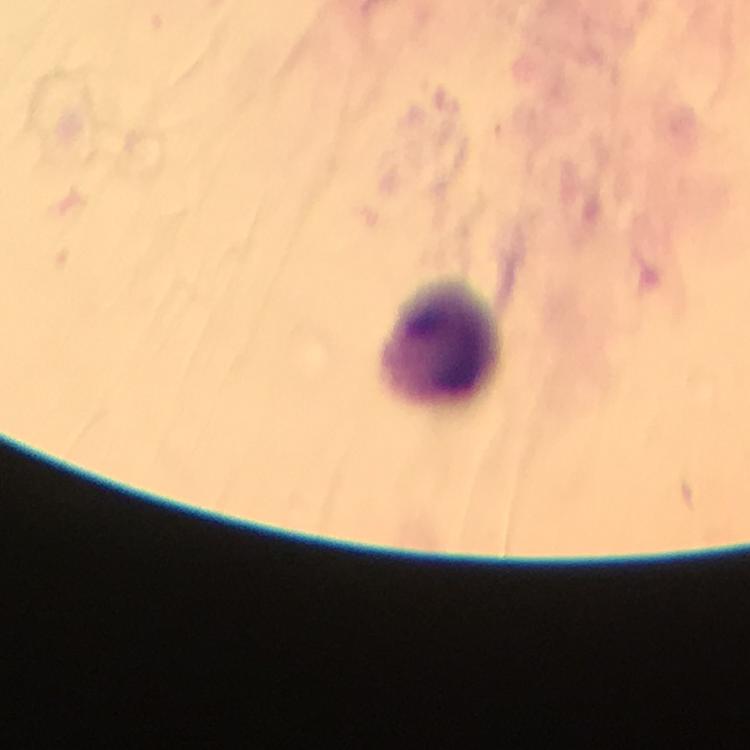

Approximate centers as {x, y} in pixels.
Summary:
  - Leukocyte locations: {441, 343}
  - Immersion oil: applied
  - Plasmodium parasites: none seen
  - Context: from a diagnostic examination for malaria
  - Capture: smartphone mounted on the microscope
  - Magnification: 100x
  - Preparation: thick blood smear
  - Stain: Giemsa
  - Cropped from: one field of view
  - Image size: 750×750 pixels